Give the location of every parasitized RBC.
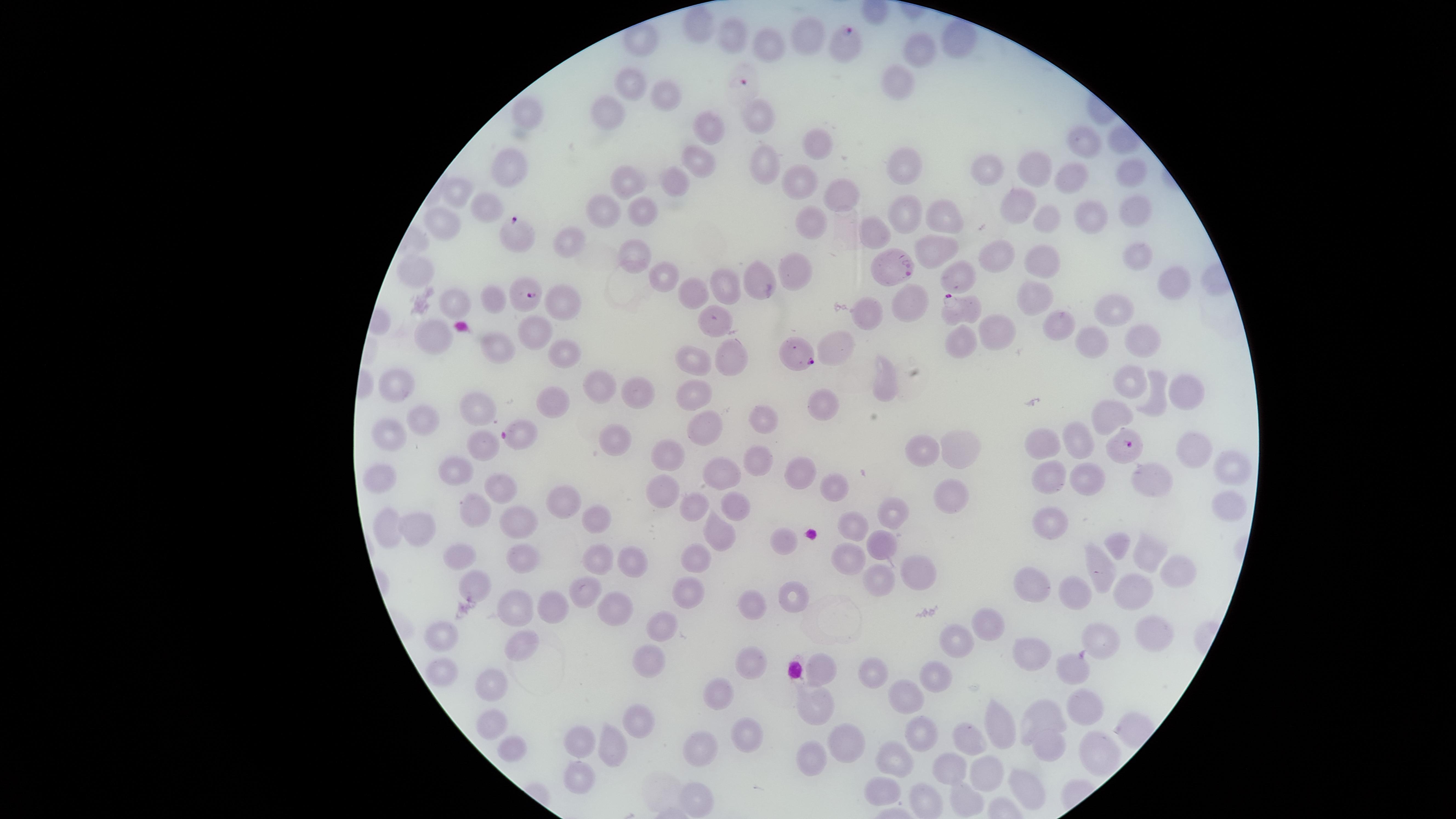
Approximate marker points as {x, y} in pixels.
Parasitized RBCs: {849, 44}, {743, 81}, {521, 237}, {893, 267}, {527, 294}, {955, 310}, {800, 353}, {519, 435}, {1131, 448}.

Approximate marker points as {x, y} in pixels. Uninfected RBCs: {700, 23}, {736, 33}, {809, 35}, {641, 39}, {952, 41}, {772, 48}, {917, 53}, {633, 80}, {894, 81}, {670, 96}, {609, 108}, {529, 118}, {757, 120}, {705, 129}, {1081, 139}, {815, 144}, {698, 160}, {765, 163}, {514, 165}, {988, 165}, {903, 168}, {1033, 169}, {1128, 174}, {1066, 179}, {630, 180}, {676, 182}, {799, 185}, {458, 191}, {839, 196}, {1012, 202}, {1134, 205}, {603, 206}, {485, 208}, {901, 210}, {641, 212}, {1093, 215}, {943, 218}, {1041, 219}, {807, 221}, {440, 223}, {872, 236}, {571, 241}, {932, 250}, {1133, 250}, {994, 254}, {633, 256}, {1039, 263}, {800, 265}, {416, 266}, {959, 275}, {663, 276}, {1168, 281}, {730, 286}, {694, 291}, {492, 296}, {450, 298}, {564, 301}, {1032, 301}, {911, 302}, {1110, 308}, {864, 314}, {1056, 323}, {993, 326}, {534, 332}, {1139, 335}, {960, 338}, {428, 339}, {1089, 340}, {496, 344}, {844, 349}, {564, 355}, {685, 359}, {728, 363}, {1130, 376}, {595, 383}, {887, 386}, {1183, 391}, {693, 392}, {396, 393}, {631, 394}, {1155, 396}, {550, 398}, {478, 408}, {819, 409}, {1109, 414}, {763, 419}, {417, 423}, {702, 426}, {388, 433}, {1075, 436}, {483, 443}, {614, 443}, {1042, 444}, {1184, 449}, {960, 451}, {662, 452}, {922, 453}, {751, 463}, {454, 465}, {1232, 465}, {801, 471}, {1083, 472}, {1153, 472}, {377, 476}, {715, 477}, {1047, 480}, {496, 481}, {838, 484}, {662, 495}, {946, 495}, {562, 499}, {1231, 504}, {697, 507}, {734, 509}, {478, 510}, {599, 517}, {891, 517}, {517, 520}, {1049, 522}, {426, 526}, {852, 528}, {387, 530}, {719, 537}, {883, 539}, {783, 541}, {1120, 545}, {1148, 549}, {844, 551}, {460, 554}, {601, 559}, {695, 559}, {523, 560}, {630, 562}, {1103, 568}, {912, 571}, {1176, 572}, {873, 575}, {1030, 583}, {474, 587}, {582, 589}, {1072, 591}, {1133, 591}, {689, 592}, {790, 593}, {752, 606}, {614, 607}, {520, 609}, {547, 609}, {660, 622}, {988, 630}, {1150, 636}, {438, 639}, {1103, 639}, {523, 644}, {961, 644}, {1032, 655}, {650, 659}, {751, 663}, {823, 663}, {439, 667}, {873, 668}, {1066, 668}, {935, 679}, {490, 682}, {718, 692}, {906, 697}, {815, 702}, {1085, 709}, {638, 713}, {1049, 713}, {487, 718}, {999, 720}, {920, 732}, {746, 733}, {971, 735}, {579, 737}, {843, 740}, {703, 741}, {510, 743}, {608, 744}, {1053, 748}, {1093, 752}, {807, 755}, {895, 758}, {950, 767}, {989, 769}, {574, 776}, {884, 784}, {1027, 787}, {699, 796}, {927, 801}, {965, 801}. Circular visible region. Image is 1456×819 pixels. One field of view of the specimen. Species: Plasmodium falciparum. Giemsa-stained preparation. Thin smear of blood. Smartphone photograph through the microscope eyepiece.